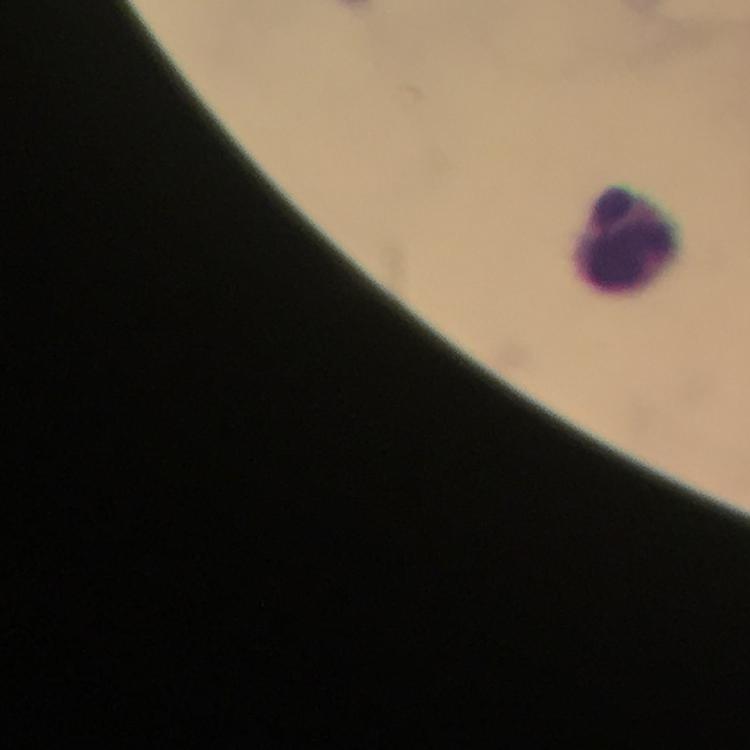

Approximate centers as (x, y) in pixels. Leukocyte locations: (629, 243). 100x magnification. Smartphone photograph taken through a microscope. Malaria parasites: none seen. From a malaria diagnostic workup. Thick smear. A crop from one field of view. Immersion oil applied. Giemsa-stained preparation. Image is 750×750 pixels.